Name the parasite shown.
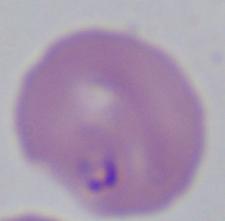
Babesia.

Summary:
  - Modality: photomicrograph
  - Magnification: 1000x